Assess the morphology of the red blood cells.
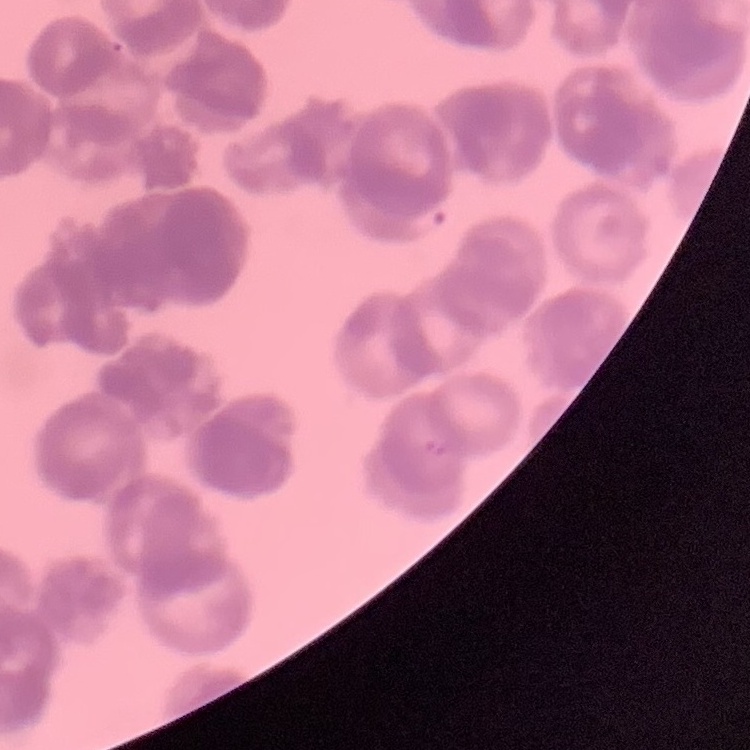

Rouleaux formation.

Stained with either Field's or Giemsa. Thin peripheral smear. One tile cut from a larger photomicrograph.